Locate every leukocyte (white blood cell).
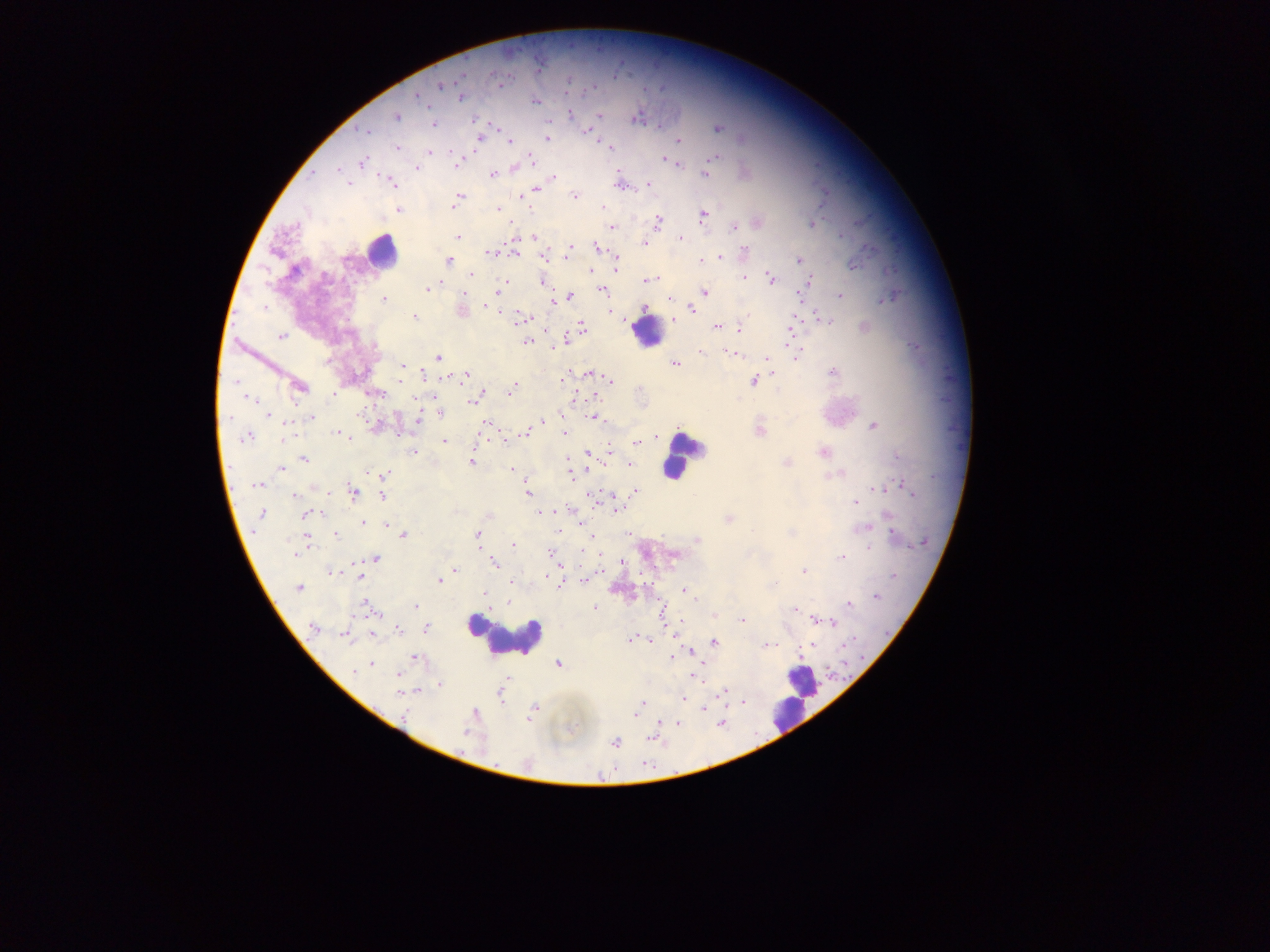

Approximate centers as [x, y] in pixels.
Leukocytes: [380, 250], [647, 331], [679, 457], [503, 637], [802, 686], [781, 716].

Summary:
  - Malaria parasite locations: [498, 83], [440, 85], [417, 95], [461, 97], [534, 101], [600, 115], [397, 117], [635, 119], [434, 124], [718, 128], [363, 131], [587, 131], [547, 138], [480, 139], [679, 141], [509, 142], [397, 148], [609, 148], [430, 151], [714, 157], [531, 158], [664, 159], [671, 161], [362, 162], [456, 164], [678, 164], [417, 167], [514, 168], [338, 169], [705, 174], [312, 175], [493, 175], [554, 177], [391, 182], [348, 183], [649, 183], [536, 189], [574, 195], [521, 197], [457, 199], [455, 204], [603, 207], [399, 209], [498, 209], [703, 215], [658, 221], [813, 224], [610, 227], [734, 227], [458, 237], [534, 238], [680, 238], [514, 240], [644, 243], [595, 247], [570, 248], [745, 250], [568, 252], [489, 253], [514, 253], [543, 257], [719, 257], [701, 260], [713, 260], [798, 260], [448, 261], [854, 265], [616, 268], [591, 271], [472, 275], [744, 277], [771, 278], [505, 280], [648, 280], [809, 281], [542, 283], [428, 289], [602, 290], [499, 291], [704, 292], [464, 293], [840, 295], [570, 296], [668, 298], [889, 298], [384, 300], [553, 302], [487, 306], [264, 308], [692, 310], [414, 317], [521, 318], [528, 318], [674, 319], [826, 320], [716, 326], [582, 327], [739, 328], [791, 329], [281, 336], [527, 341], [735, 349], [792, 349], [701, 352], [732, 353], [795, 355], [438, 357], [767, 358], [675, 364], [403, 366], [590, 373], [773, 373], [832, 373], [424, 374], [466, 375], [565, 378], [610, 381], [754, 381], [300, 387], [512, 389], [482, 394], [250, 398], [472, 402], [441, 414], [269, 416], [311, 417], [594, 417], [418, 419], [543, 422], [485, 425], [873, 426], [525, 431], [760, 431], [339, 434], [564, 434], [284, 436], [247, 437], [345, 437], [657, 437], [444, 441], [636, 442], [413, 452], [824, 452], [898, 457], [304, 458], [472, 461], [786, 463], [630, 464], [281, 468], [512, 469], [571, 472], [383, 474], [834, 476], [257, 485], [907, 487], [875, 490], [635, 491], [527, 492], [353, 493], [382, 496], [294, 497], [596, 497], [856, 503], [617, 508], [540, 513], [546, 513], [261, 514], [314, 514], [307, 515], [888, 516], [729, 519], [363, 523], [386, 526], [865, 528], [753, 530], [559, 531], [791, 533], [403, 534], [477, 534], [627, 534], [336, 535], [894, 535], [590, 537], [697, 540], [513, 545], [868, 548], [295, 553], [550, 553], [843, 557], [375, 559], [623, 562], [493, 563], [455, 570], [804, 571], [333, 572], [546, 576], [894, 576], [359, 577], [439, 580], [585, 580], [511, 583], [560, 584], [299, 588], [685, 591], [485, 593], [876, 596], [849, 603], [416, 605], [370, 608], [595, 608], [795, 610], [714, 616], [814, 619], [741, 620], [833, 622], [313, 628], [426, 628], [399, 629], [346, 635], [647, 639], [631, 640], [713, 642], [768, 645], [812, 645], [690, 651], [672, 657], [414, 658], [370, 664], [559, 664], [362, 667], [355, 670], [398, 675], [694, 676], [439, 686], [725, 690], [400, 692], [684, 699], [641, 703], [704, 708], [535, 709], [637, 710], [405, 714], [530, 718], [677, 723], [721, 723], [615, 742]
  - Image size: 1270×952 pixels
  - Country: Ghana
  - Capture: mobile-phone photograph through a microscope
  - Field of view: single
  - Preparation: thick blood smear